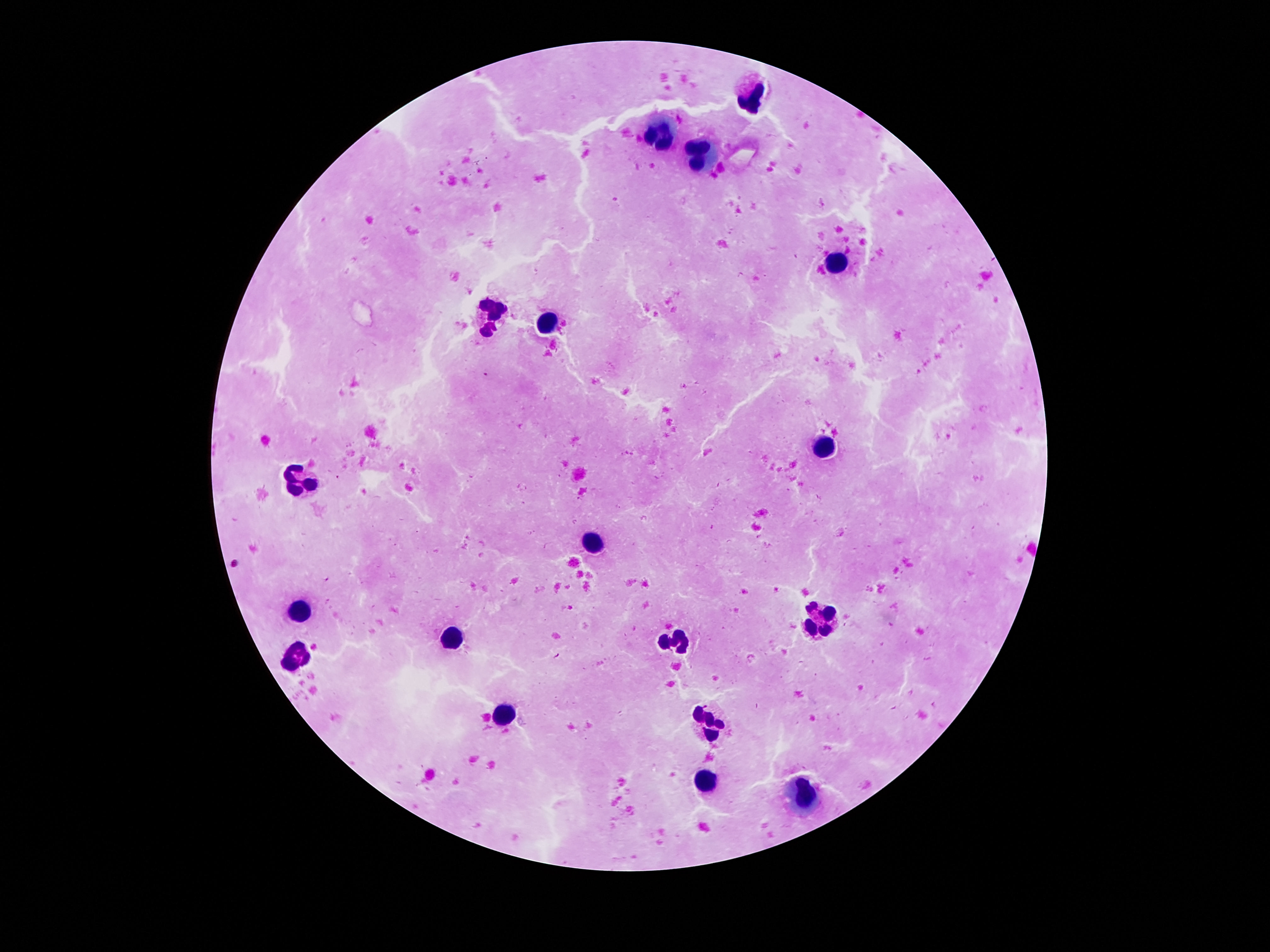

magnification = 100x
stain = Giemsa
image size = 1270×952 pixels
leukocyte locations = approximate object centers, in pixels from the top-left corner: (x=748, y=95), (x=661, y=133), (x=699, y=153), (x=835, y=267), (x=489, y=314), (x=549, y=323), (x=827, y=445), (x=301, y=479), (x=593, y=543), (x=298, y=609), (x=822, y=620), (x=451, y=640), (x=677, y=640), (x=298, y=654), (x=504, y=711), (x=717, y=726), (x=705, y=783), (x=806, y=797)
field of view = one from this slide
capture = smartphone camera through the microscope eyepiece
preparation = thick blood film
patient malaria status = uninfected